Identify the parasite.
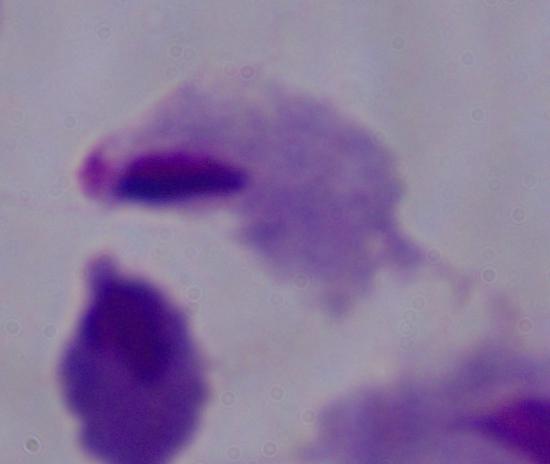
A trichomonad.

Micrograph. Captured at 1000x magnification.